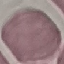
Result: negative for malaria parasites. Giemsa-stained preparation. Cell patch, automatically extracted from a larger field of view and resized to 64 × 64 pixels. Acquired by smartphone through the microscope eyepiece. Thin blood smear.